Locate leukocytes (white blood cells).
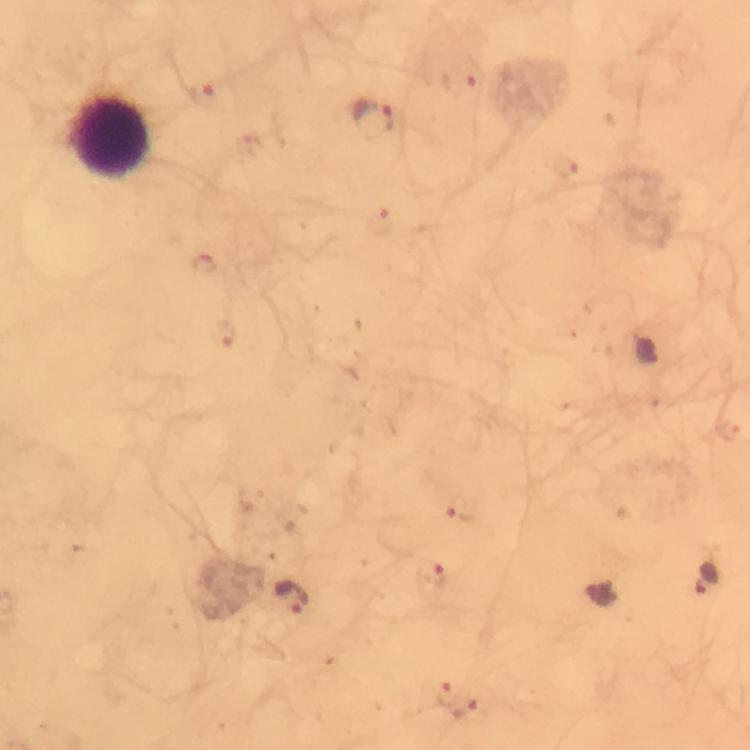
Approximate centers as {x, y} in pixels.
Leukocytes: {112, 138}.

Plasmodium parasite locations: {459, 82}, {207, 94}, {373, 119}, {564, 168}, {380, 223}, {204, 264}, {223, 334}, {463, 508}, {431, 577}, {708, 580}, {291, 596}, {602, 597}, {447, 691}, {465, 708}. A crop from one field of view. Immersion oil was used. Photographed with a smartphone mounted on the microscope. Thick smear. Image is 750×750 pixels. From a malaria diagnostic workup. Giemsa stain. 100x magnification.